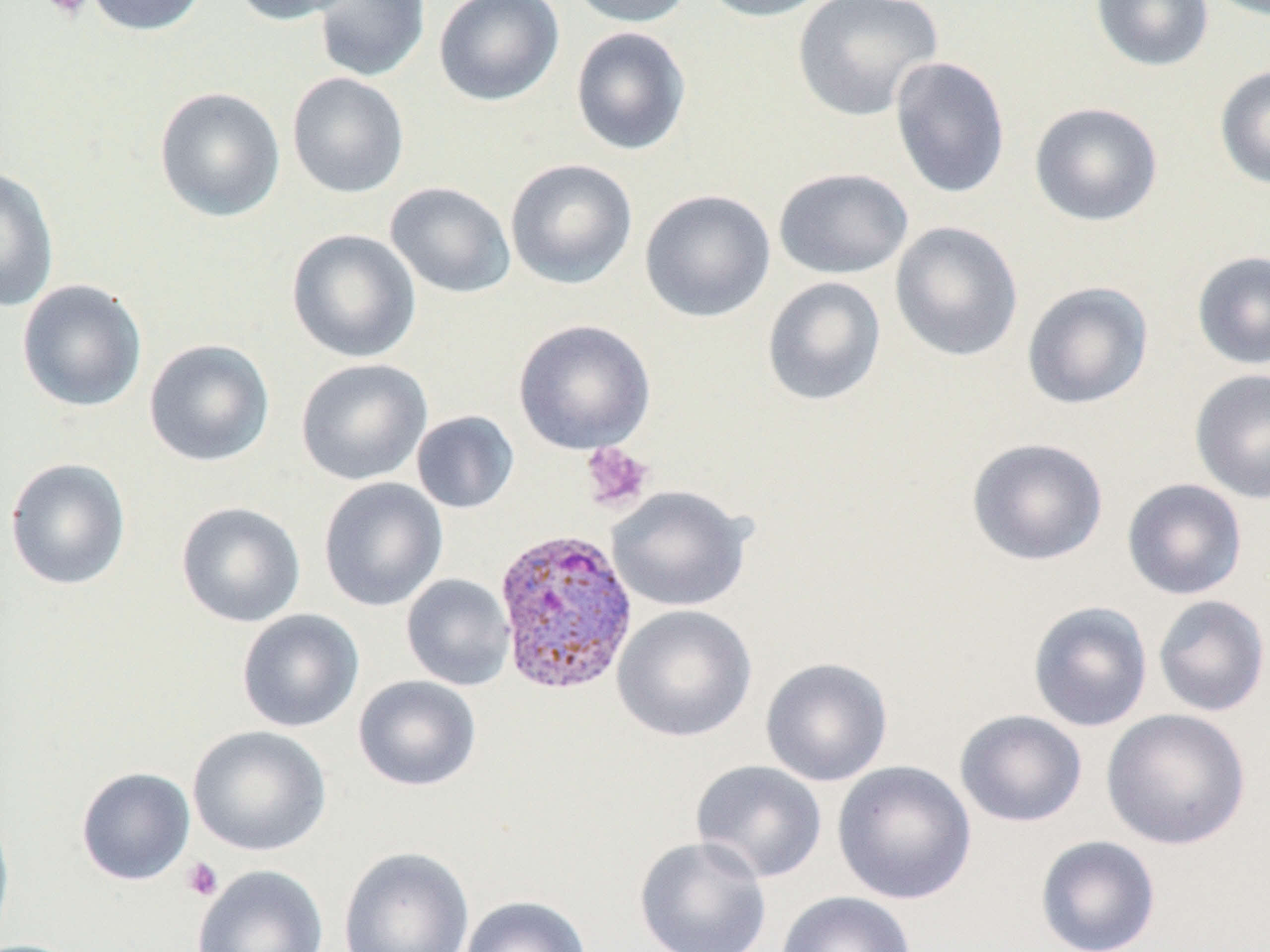

Summary:
  - Coordinate format: approximate bounding boxes as (x1, y1, x2, y2) in pixels
  - Uninfected red blood cell locations: (84, 0, 209, 36), (230, 0, 359, 25), (312, 0, 430, 82), (434, 0, 564, 106), (566, 0, 694, 28), (696, 0, 835, 22), (792, 0, 943, 122), (1090, 0, 1214, 72), (570, 26, 692, 156), (889, 55, 1011, 200), (1214, 65, 1270, 191), (287, 73, 409, 198), (154, 86, 286, 222), (1029, 101, 1163, 227), (505, 158, 638, 289), (0, 166, 59, 313), (773, 167, 913, 280), (385, 181, 516, 299), (639, 189, 775, 323), (889, 221, 1023, 361), (286, 229, 421, 363), (1191, 250, 1270, 370), (761, 276, 887, 406), (16, 279, 148, 412), (1021, 281, 1154, 410), (513, 319, 656, 455), (143, 338, 276, 467), (296, 358, 433, 486), (1189, 368, 1270, 504), (411, 410, 520, 514), (966, 437, 1108, 566), (4, 458, 131, 590), (318, 477, 448, 612), (1121, 478, 1248, 600), (606, 486, 753, 612), (176, 501, 306, 628), (401, 573, 515, 691), (1152, 594, 1270, 717), (1027, 600, 1153, 733), (612, 604, 757, 742), (236, 609, 364, 733), (760, 657, 893, 786), (352, 675, 483, 792), (1101, 708, 1252, 850), (954, 709, 1088, 827), (187, 725, 331, 856), (690, 759, 828, 883), (831, 760, 977, 905), (75, 766, 195, 886), (0, 805, 15, 949), (634, 835, 772, 952), (1035, 835, 1161, 952), (337, 846, 475, 952), (192, 864, 330, 952), (774, 890, 917, 952), (459, 894, 592, 952)
  - Plasmodium vivax-infected red blood cell locations: (492, 526, 639, 696)
  - Platelet locations: (40, 0, 92, 20), (580, 442, 654, 512), (182, 857, 223, 902)
  - Slide-level diagnosis: Plasmodium vivax
  - Field of view: one of a larger specimen
  - Preparation: thin blood film
  - Magnification: 1000x
  - Image size: 1270×952 pixels
  - Stain: May-Grünwald-Giemsa
  - Modality: light microscopy